Describe the morphology of the red blood cells.
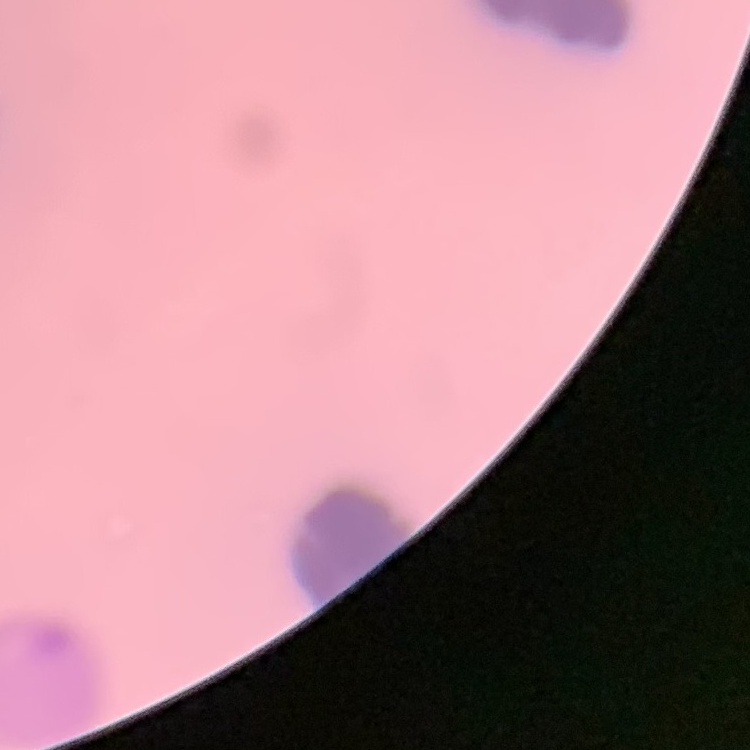
They show rouleaux formation.

Summary:
  - Image type: square crop of a larger photomicrograph
  - Preparation: thin peripheral smear
  - Stain: Field's or Giemsa